Name the cell type shown.
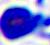
This is a leukocyte.

400x magnification. Micrograph.